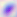
Toxoplasma gondii is seen. Micrograph. Captured at 400x magnification.